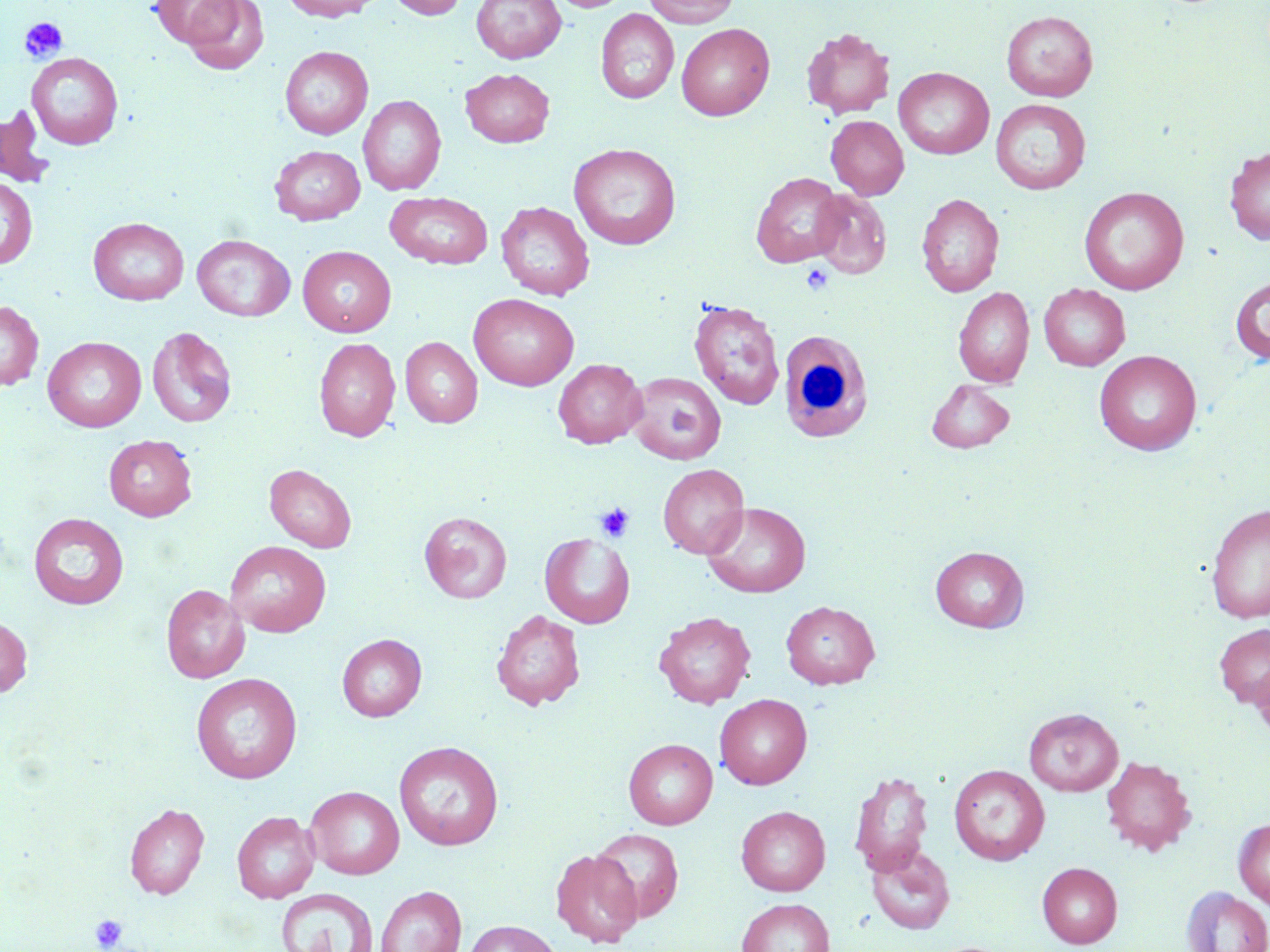

Approximate bounding boxes as (x1, y1, x2, y2) in pixels. Platelet locations: (19, 17, 68, 63), (800, 263, 834, 296), (596, 503, 635, 542), (90, 914, 128, 951). White blood cell locations: (778, 330, 875, 443). Uninfected red blood cell locations: (150, 0, 242, 50), (181, 0, 269, 75), (281, 0, 381, 21), (387, 0, 467, 20), (472, 0, 566, 64), (550, 0, 632, 12), (643, 0, 740, 27), (596, 9, 679, 104), (1001, 10, 1098, 101), (676, 23, 775, 120), (801, 27, 894, 118), (280, 46, 373, 139), (26, 53, 124, 150), (894, 67, 994, 159), (460, 68, 555, 147), (358, 94, 446, 196), (991, 99, 1091, 194), (0, 105, 55, 188), (826, 115, 909, 199), (568, 143, 682, 250), (270, 145, 365, 225), (1224, 146, 1270, 246), (751, 172, 844, 268), (0, 176, 37, 270), (1079, 187, 1189, 295), (811, 190, 892, 278), (385, 192, 493, 269), (916, 193, 1004, 297), (496, 201, 594, 300), (88, 217, 189, 305), (192, 235, 295, 321), (298, 246, 396, 337), (1230, 275, 1270, 365), (1039, 283, 1130, 371), (953, 286, 1034, 387), (468, 293, 579, 390), (688, 298, 784, 409), (0, 300, 43, 390), (147, 326, 237, 429), (42, 336, 146, 432), (314, 337, 400, 442), (400, 337, 482, 428), (1094, 350, 1201, 455), (553, 358, 647, 448), (627, 372, 726, 464), (926, 379, 1015, 453), (103, 434, 197, 520), (264, 463, 357, 552), (657, 464, 749, 559), (702, 502, 811, 598), (1206, 503, 1270, 624), (420, 511, 512, 603), (28, 512, 129, 609), (539, 532, 635, 628), (226, 540, 331, 637), (930, 546, 1029, 632), (161, 584, 249, 683), (781, 601, 880, 689), (491, 609, 585, 711), (653, 611, 756, 708), (0, 615, 32, 697), (1214, 623, 1270, 709), (337, 634, 427, 721), (1252, 656, 1270, 740), (191, 673, 302, 783), (715, 693, 812, 789), (1024, 707, 1123, 796), (623, 738, 717, 829), (394, 740, 504, 850), (1100, 755, 1195, 855), (948, 763, 1050, 865), (849, 770, 934, 877), (305, 785, 404, 879), (124, 802, 209, 899), (736, 805, 830, 896), (231, 810, 319, 903), (1233, 818, 1270, 909), (591, 828, 684, 922), (865, 845, 956, 935), (550, 849, 643, 947), (1037, 862, 1123, 948), (375, 885, 466, 952), (1181, 887, 1270, 952), (276, 888, 379, 952), (736, 897, 835, 952), (461, 920, 563, 952). Slide-level diagnosis: negative for blood parasites. Single field of view. Optical microscopy. Captured at 1000x magnification. Image is 1270×952 pixels. May-Grünwald-Giemsa stain. Thin blood film.